Locate every Plasmodium falciparum-infected red blood cell.
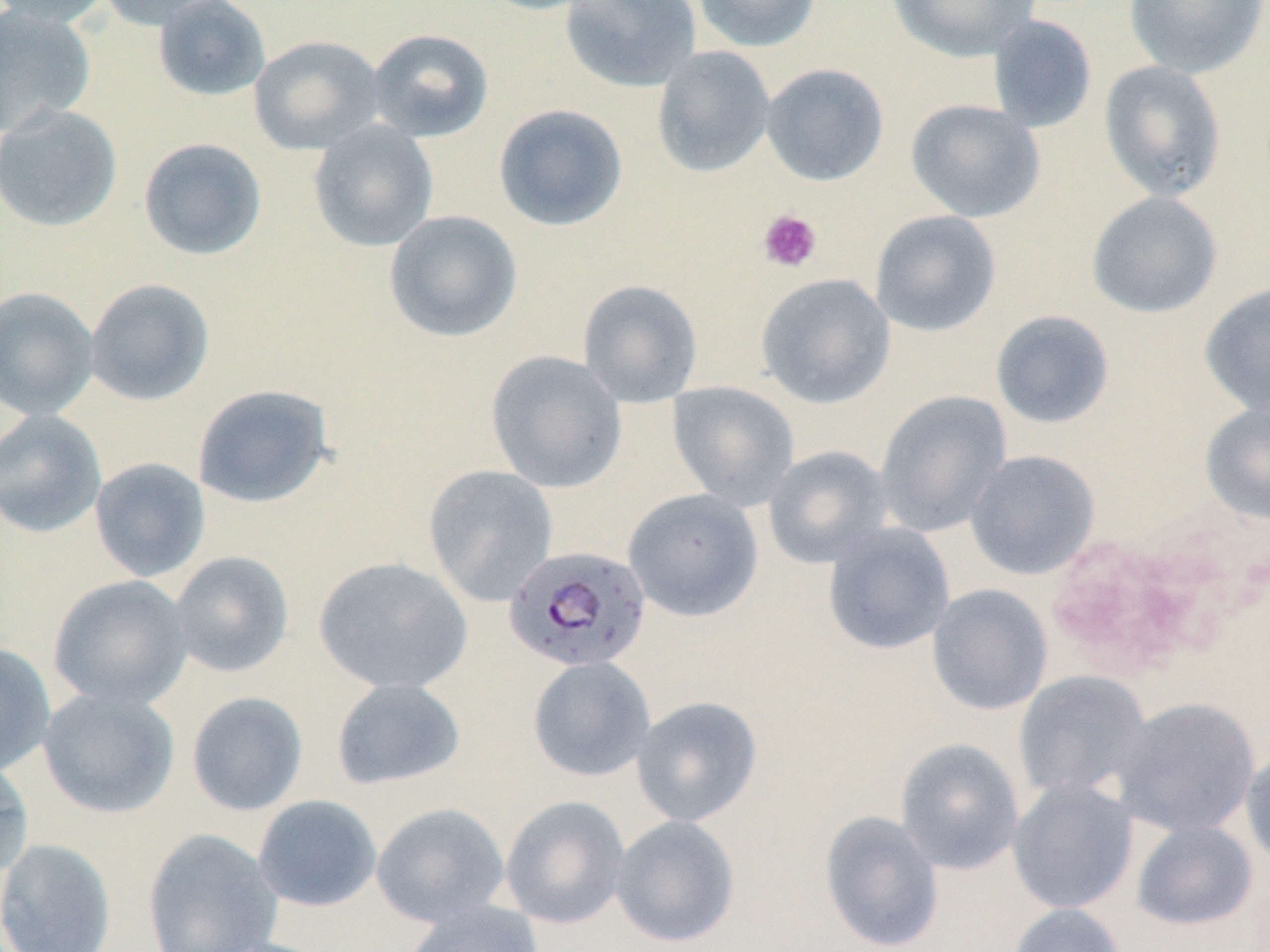
Approximate bounding boxes as [x1, y1, x2, y2] in pixels.
Plasmodium falciparum-infected red blood cells: [503, 545, 652, 674].

slide-level diagnosis = Plasmodium falciparum
platelet locations = approximate bounding boxes as [x1, y1, x2, y2] in pixels: [757, 209, 822, 273]
magnification = 1000x
field of view = one of a larger specimen
preparation = thin blood smear
stain = May-Grünwald-Giemsa
uninfected red blood cell locations = approximate bounding boxes as [x1, y1, x2, y2] in pixels: [0, 0, 116, 27], [95, 0, 230, 31], [153, 0, 271, 102], [475, 0, 608, 16], [559, 0, 702, 92], [692, 0, 822, 53], [887, 0, 1042, 62], [1124, 0, 1268, 79], [0, 4, 96, 136], [986, 15, 1098, 134], [366, 27, 495, 143], [248, 34, 387, 155], [651, 46, 776, 177], [1098, 60, 1227, 203], [760, 63, 889, 186], [905, 98, 1046, 223], [0, 102, 122, 232], [493, 104, 628, 231], [307, 121, 439, 252], [138, 137, 267, 261], [1086, 191, 1223, 319], [384, 209, 522, 343], [869, 209, 1002, 337], [755, 273, 895, 409], [83, 278, 215, 406], [577, 279, 703, 407], [1200, 281, 1270, 417], [0, 287, 100, 421], [990, 309, 1115, 429], [484, 350, 627, 494], [666, 381, 800, 510], [192, 383, 334, 508], [874, 390, 1012, 538], [1199, 399, 1270, 526], [0, 410, 107, 538], [763, 445, 893, 569], [964, 449, 1100, 580], [89, 457, 211, 582], [422, 464, 559, 607], [623, 488, 763, 621], [822, 523, 955, 655], [168, 551, 295, 678], [313, 556, 473, 694], [47, 574, 194, 710], [926, 584, 1053, 716], [0, 642, 56, 777], [527, 656, 656, 782], [1013, 671, 1152, 803], [331, 678, 466, 790], [37, 687, 180, 818], [186, 690, 309, 816], [631, 695, 763, 826], [1111, 696, 1260, 838], [895, 738, 1025, 875], [1240, 745, 1270, 870], [0, 759, 34, 880], [1007, 777, 1139, 914], [253, 795, 382, 911], [500, 795, 630, 929], [371, 802, 510, 927], [819, 810, 944, 951], [610, 814, 740, 948], [1130, 820, 1259, 932], [142, 828, 282, 952], [0, 838, 116, 952], [403, 899, 545, 952], [1007, 903, 1129, 952], [204, 937, 338, 952]
modality = light microscopy
image size = 1270×952 pixels